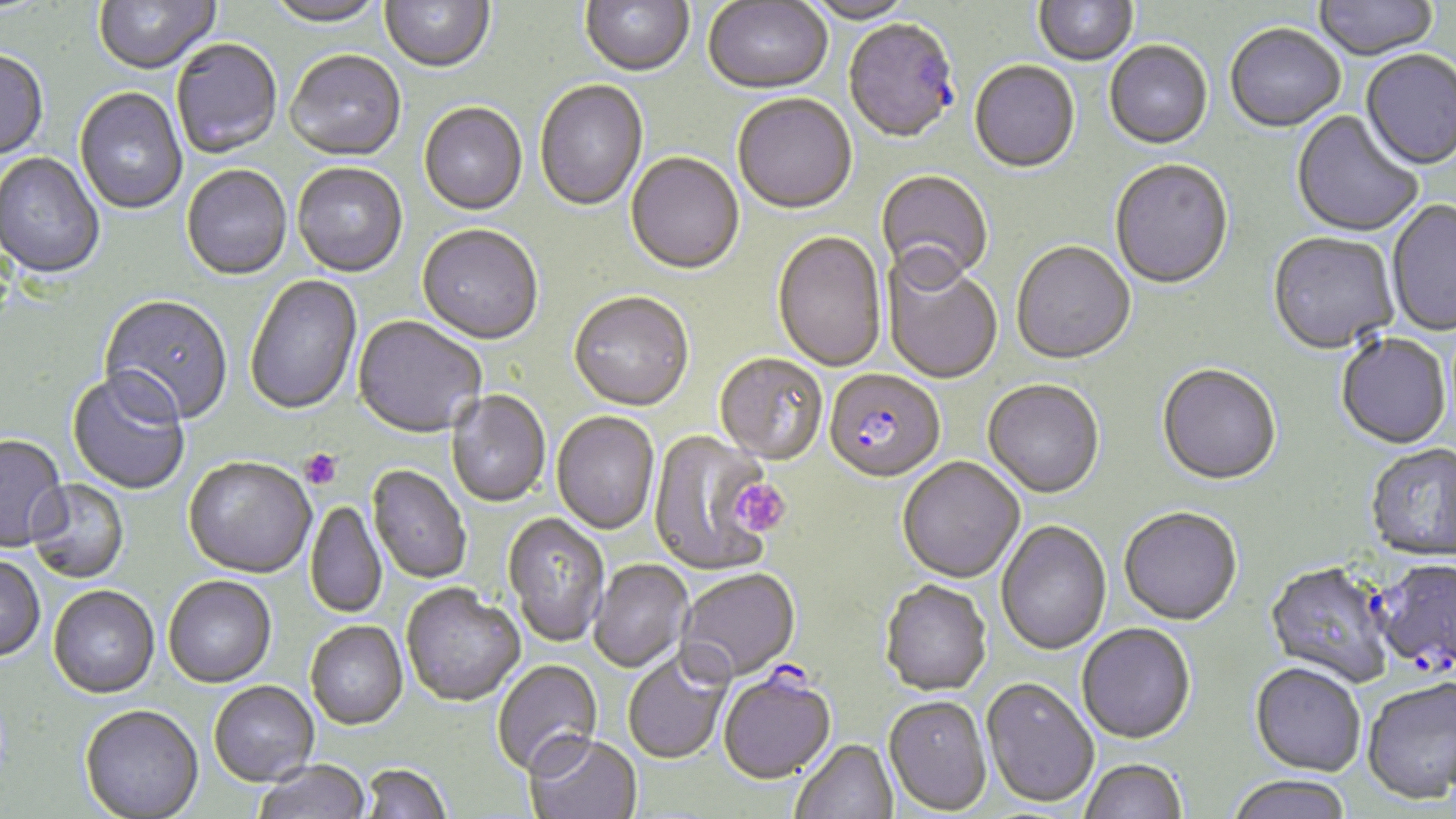
slide-level diagnosis = Plasmodium falciparum
image size = 1456×819 pixels
uninfected red blood cell locations = approximate bounding boxes as (x1, y1, x2, y2) in pixels: (93, 0, 221, 76), (265, 0, 387, 29), (380, 0, 495, 75), (580, 0, 694, 79), (1034, 0, 1138, 68), (1314, 0, 1439, 63), (703, 1, 833, 97), (803, 1, 918, 26), (1225, 26, 1346, 134), (171, 40, 282, 160), (1104, 43, 1213, 151), (0, 51, 49, 162), (1360, 51, 1456, 173), (284, 52, 406, 164), (969, 62, 1080, 176), (535, 80, 649, 213), (75, 88, 187, 216), (732, 95, 857, 216), (418, 104, 528, 217), (1291, 111, 1423, 239), (0, 153, 105, 280), (625, 154, 744, 277), (1110, 161, 1234, 291), (292, 164, 408, 279), (182, 166, 292, 282), (876, 170, 993, 290), (1386, 200, 1456, 338), (417, 226, 543, 347), (772, 232, 886, 374), (1267, 234, 1399, 357), (1011, 243, 1136, 366), (883, 260, 1003, 385), (244, 274, 363, 417), (568, 294, 694, 414), (98, 296, 234, 429), (353, 316, 487, 440), (1336, 335, 1451, 450), (714, 355, 828, 467), (1157, 366, 1281, 487), (67, 373, 190, 495), (983, 381, 1105, 500), (446, 391, 550, 508), (551, 413, 660, 536), (648, 429, 778, 576), (0, 435, 69, 554), (1365, 445, 1456, 563), (897, 458, 1025, 585), (183, 459, 316, 580), (368, 466, 470, 584), (25, 478, 130, 584), (305, 501, 387, 619), (1119, 509, 1242, 627), (502, 513, 609, 648), (996, 521, 1112, 656), (0, 556, 45, 664), (1370, 558, 1456, 676), (590, 560, 692, 673), (1265, 563, 1394, 687), (677, 570, 801, 684), (163, 577, 277, 689), (879, 581, 991, 698), (401, 585, 525, 709), (48, 587, 159, 701), (305, 622, 408, 731), (1077, 624, 1195, 745), (623, 651, 731, 765), (492, 661, 603, 779), (1250, 663, 1366, 777), (1362, 678, 1456, 804), (981, 679, 1099, 809), (209, 682, 319, 789), (883, 696, 992, 816), (79, 707, 204, 819), (525, 736, 643, 819), (790, 740, 898, 819), (1080, 760, 1186, 819), (254, 761, 370, 819), (361, 765, 451, 819), (1226, 776, 1353, 819)
Plasmodium falciparum-infected red blood cell locations = approximate bounding boxes as (x1, y1, x2, y2) in pixels: (843, 21, 959, 146), (825, 372, 944, 484), (718, 658, 836, 786)
preparation = thin blood film
modality = light microscopy
magnification = 1000x
stain = May-Grünwald-Giemsa
platelet locations = approximate bounding boxes as (x1, y1, x2, y2) in pixels: (299, 449, 343, 490), (732, 480, 790, 536)
field of view = one of a larger specimen